Outline each blood parasite and name the species.
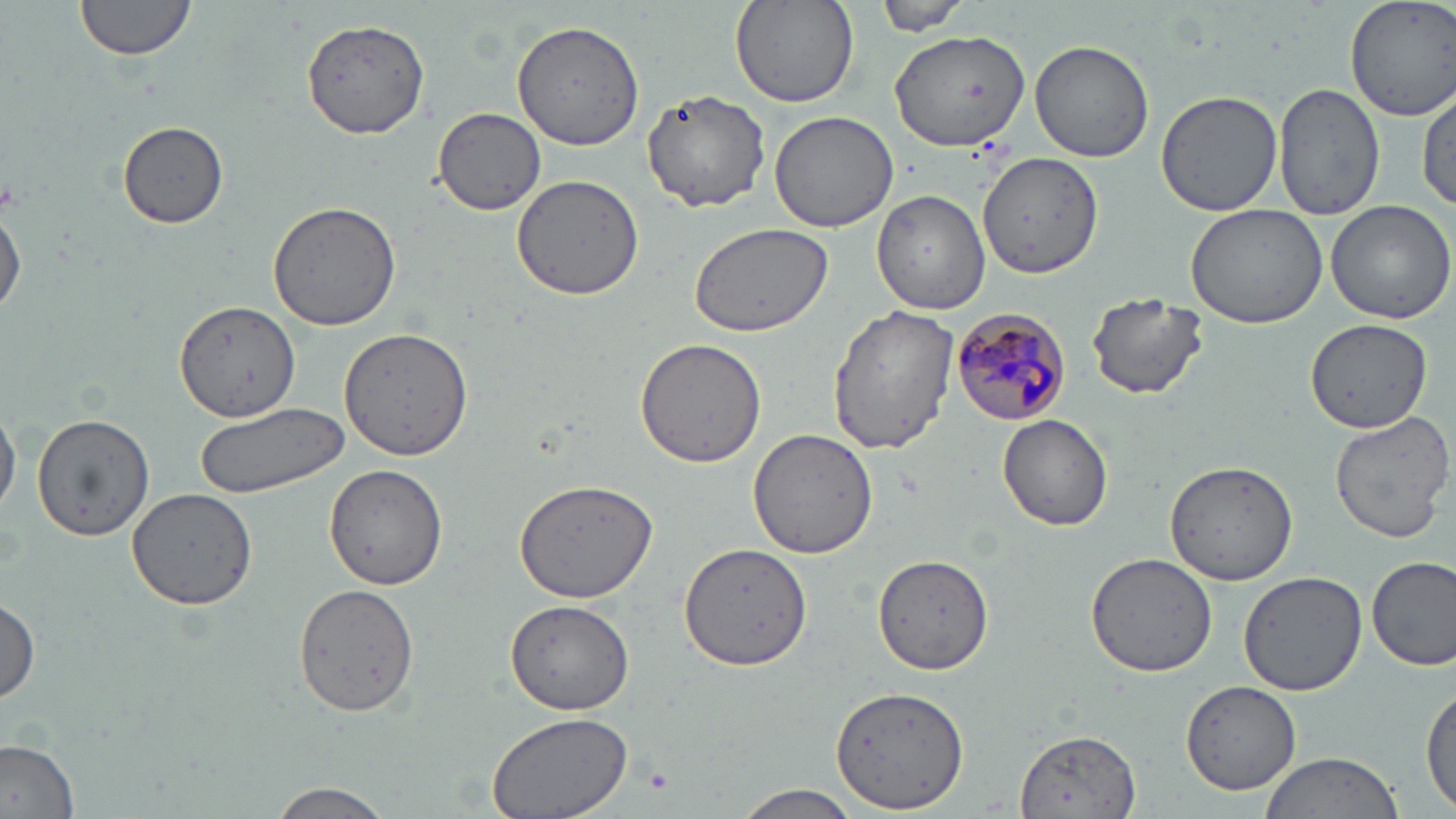
Approximate bounding boxes as named x1/y1/x2/y2 corners in pixels.
Plasmodium malariae-infected red blood cells: (x1=950, y1=305, x2=1072, y2=424).
No Plasmodium falciparum, Plasmodium ovale, Plasmodium vivax, Babesia divergens, or Trypanosoma brucei observed.

slide-level diagnosis = Plasmodium malariae
modality = optical microscopy
field of view = single
image size = 1456×819 pixels
platelet locations = approximate bounding boxes as named x1/y1/x2/y2 corners in pixels: (x1=643, y1=764, x2=674, y2=794)
magnification = 1000x
preparation = thin blood smear
uninfected red blood cell locations = approximate bounding boxes as named x1/y1/x2/y2 corners in pixels: (x1=73, y1=0, x2=199, y2=66), (x1=1343, y1=0, x2=1456, y2=121), (x1=729, y1=1, x2=860, y2=110), (x1=873, y1=1, x2=969, y2=36), (x1=300, y1=18, x2=431, y2=138), (x1=510, y1=21, x2=645, y2=151), (x1=888, y1=30, x2=1032, y2=150), (x1=1030, y1=40, x2=1155, y2=164), (x1=1274, y1=84, x2=1386, y2=222), (x1=1417, y1=86, x2=1454, y2=213), (x1=641, y1=88, x2=770, y2=211), (x1=1156, y1=91, x2=1282, y2=216), (x1=432, y1=108, x2=547, y2=214), (x1=768, y1=110, x2=898, y2=233), (x1=118, y1=121, x2=227, y2=229), (x1=977, y1=151, x2=1102, y2=281), (x1=510, y1=174, x2=644, y2=300), (x1=873, y1=190, x2=993, y2=315), (x1=1325, y1=198, x2=1456, y2=324), (x1=0, y1=200, x2=25, y2=320), (x1=267, y1=200, x2=405, y2=332), (x1=1184, y1=203, x2=1328, y2=327), (x1=688, y1=220, x2=834, y2=338), (x1=1087, y1=292, x2=1210, y2=399), (x1=175, y1=299, x2=299, y2=424), (x1=828, y1=305, x2=960, y2=455), (x1=1305, y1=319, x2=1432, y2=432), (x1=339, y1=326, x2=476, y2=464), (x1=634, y1=336, x2=769, y2=470), (x1=0, y1=401, x2=20, y2=520), (x1=194, y1=402, x2=348, y2=500), (x1=1328, y1=411, x2=1455, y2=543), (x1=32, y1=413, x2=157, y2=541), (x1=997, y1=414, x2=1115, y2=531), (x1=747, y1=428, x2=880, y2=558), (x1=1162, y1=458, x2=1301, y2=586), (x1=324, y1=465, x2=450, y2=589), (x1=514, y1=478, x2=658, y2=603), (x1=126, y1=486, x2=258, y2=609), (x1=680, y1=543, x2=812, y2=672), (x1=875, y1=553, x2=992, y2=678), (x1=1085, y1=554, x2=1219, y2=678), (x1=1367, y1=555, x2=1456, y2=671), (x1=1237, y1=572, x2=1369, y2=696), (x1=293, y1=581, x2=419, y2=717), (x1=0, y1=597, x2=41, y2=703), (x1=504, y1=599, x2=636, y2=715), (x1=1180, y1=683, x2=1301, y2=793), (x1=1419, y1=685, x2=1455, y2=813), (x1=832, y1=687, x2=970, y2=810), (x1=481, y1=709, x2=632, y2=819), (x1=1016, y1=728, x2=1141, y2=818), (x1=0, y1=740, x2=80, y2=817), (x1=1259, y1=751, x2=1406, y2=819), (x1=263, y1=781, x2=397, y2=818), (x1=731, y1=784, x2=863, y2=818)
stain = May-Grünwald-Giemsa